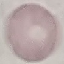

malaria status = uninfected
stain = Giemsa
preparation = thin smear
image type = automatically extracted cell patch, resized to 64 × 64 pixels
capture = smartphone camera at the microscope eyepiece